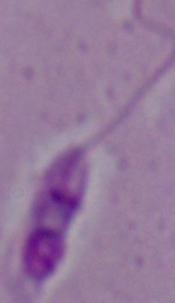
Summary:
  - Identification: Leishmania
  - Modality: micrograph
  - Magnification: 1000x